Assess this cell for malaria.
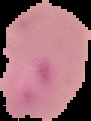

Parasitized.

image type = segmented cell region on a black background
image size = 91×121 pixels
preparation = thin blood smear